Name the parasite shown.
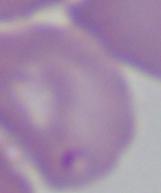

Babesia.

Summary:
  - Magnification: 1000x
  - Modality: micrograph